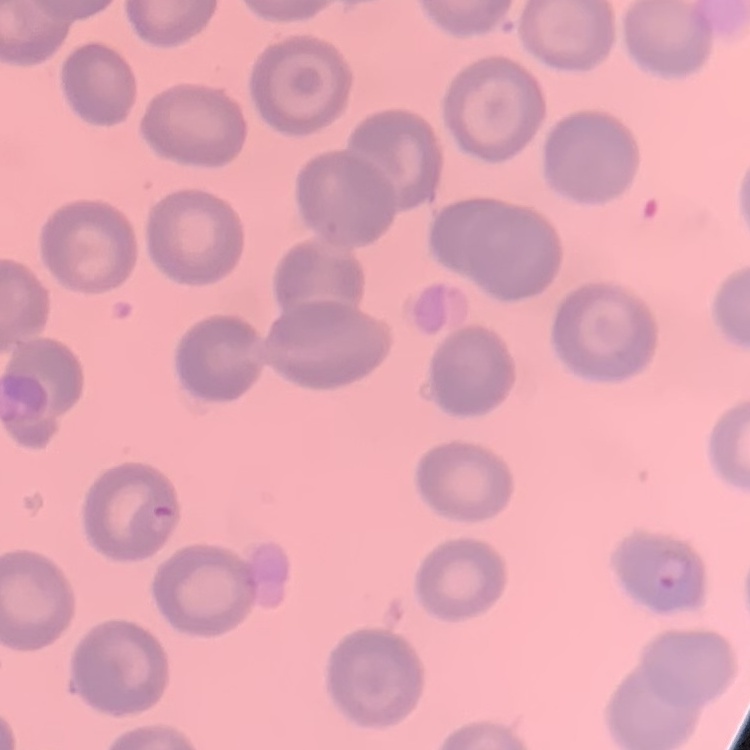

The red blood cells exhibit no rouleaux formation. Stained with either Field's or Giemsa. Thin blood film. One tile cut from a larger photomicrograph.